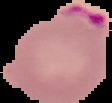

Summary:
  - Image type: cell region segmented out of the field of view; surrounding area masked to black
  - Preparation: thin blood smear
  - Result: Plasmodium parasites detected
  - Image size: 112×103 pixels